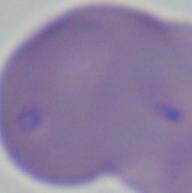

Summary:
  - Identification: Babesia
  - Modality: photomicrograph
  - Magnification: 1000x